Comment on the morphology of the red blood cells.
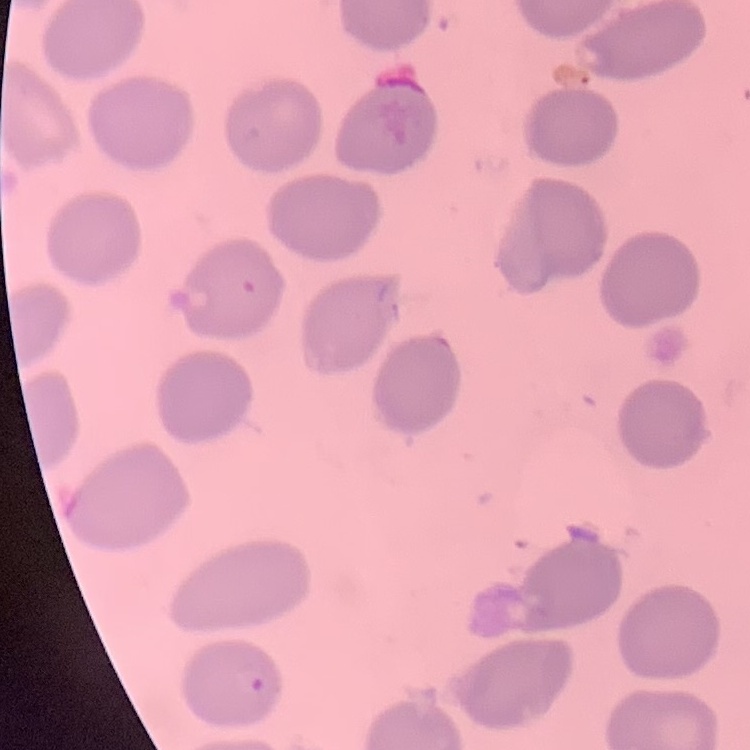
They show no rouleaux formation.

stain = Field's or Giemsa
image type = square crop of a larger photomicrograph
preparation = thin blood smear